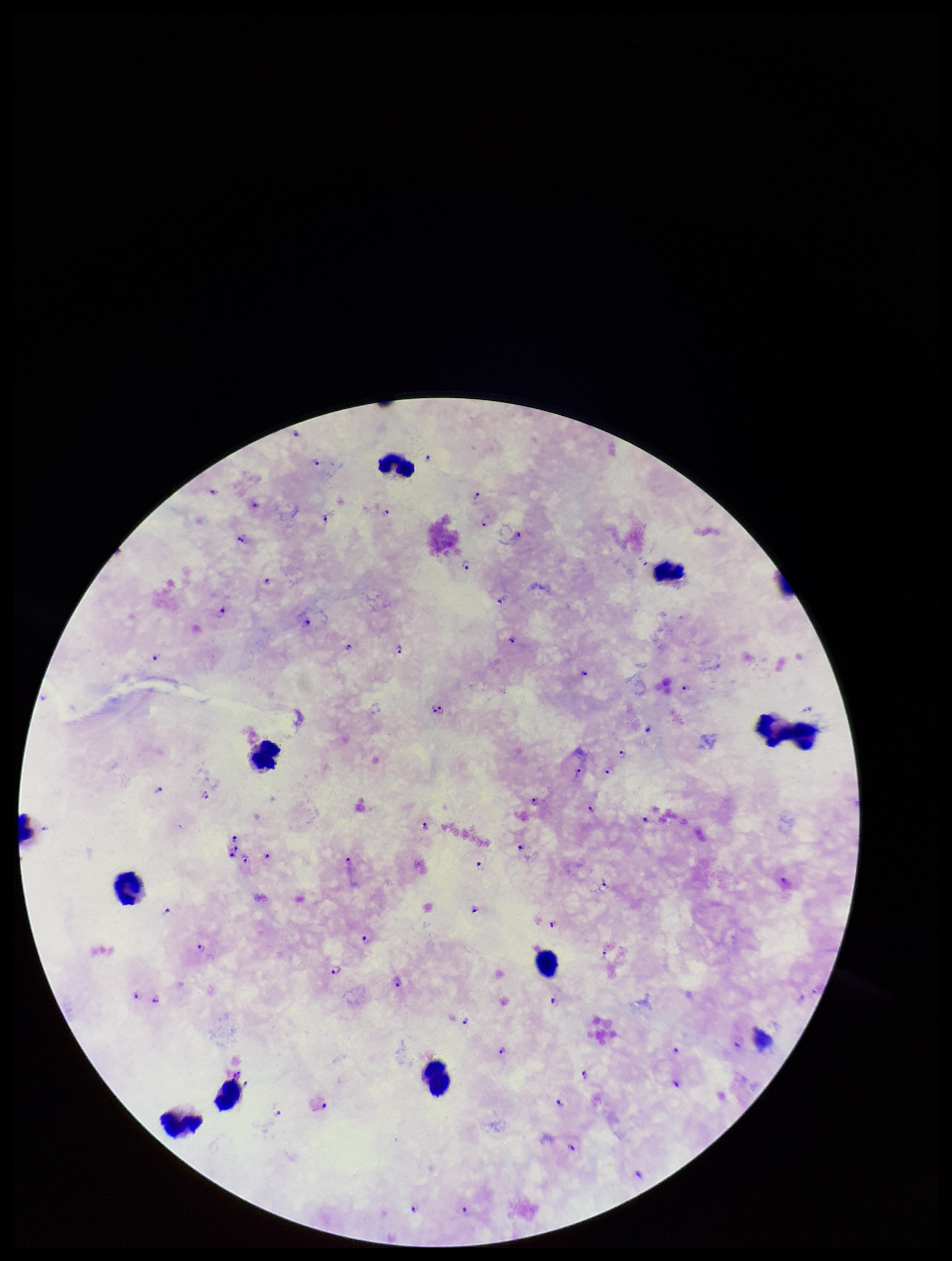
Single field of view. Plasmodium parasites: identified. Image is 952×1261 pixels. Preparation: thick smear. Leukocyte count: 10. Species reported for this patient: Plasmodium falciparum. Parasite count: 75. Patient malaria status: positive. Photographed through the microscope eyepiece with a smartphone camera. Stained with Giemsa.